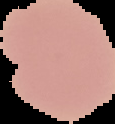
Summary:
  - Image size: 115×124 pixels
  - Image type: segmented cell region on a black background
  - Result: no malaria parasites seen
  - Preparation: thin blood film